Classify this cell by malaria status.
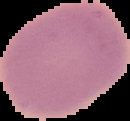
Uninfected.

image size = 130×121 pixels
preparation = thin blood smear
image type = segmented cell region with the area outside set to black